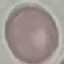 Result: no malaria parasites detected. Acquired by smartphone through the microscope eyepiece. Thin smear of blood. Automatically extracted cell patch, resized to 64 × 64 pixels. Giemsa-stained preparation.